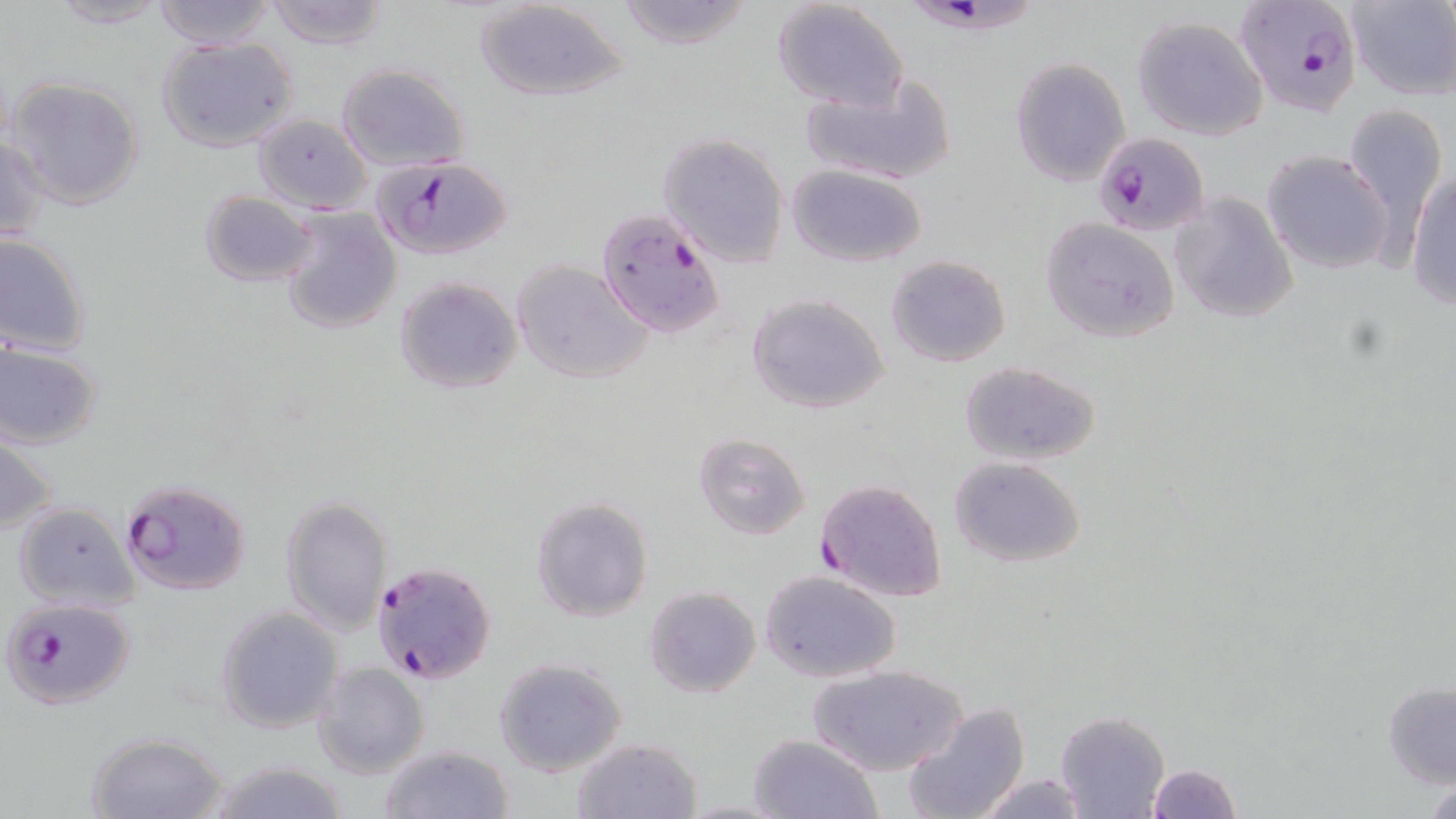
slide-level diagnosis = Plasmodium falciparum
modality = light microscopy
stain = May-Grünwald-Giemsa
magnification = 1000x
Plasmodium falciparum-infected red blood cell locations = approximate bounding boxes as named x1/y1/x2/y2 corners in pixels: (x1=910, y1=0, x2=1036, y2=40), (x1=1238, y1=0, x2=1364, y2=115), (x1=1098, y1=126, x2=1212, y2=239), (x1=373, y1=154, x2=516, y2=260), (x1=596, y1=207, x2=725, y2=338), (x1=814, y1=477, x2=948, y2=603), (x1=119, y1=479, x2=251, y2=597), (x1=369, y1=557, x2=496, y2=685), (x1=2, y1=597, x2=134, y2=710)
preparation = thin blood smear
image size = 1456×819 pixels
field of view = single
uninfected red blood cell locations = approximate bounding boxes as named x1/y1/x2/y2 corners in pixels: (x1=45, y1=0, x2=171, y2=28), (x1=151, y1=0, x2=277, y2=49), (x1=264, y1=0, x2=387, y2=49), (x1=472, y1=0, x2=631, y2=105), (x1=614, y1=0, x2=756, y2=50), (x1=1344, y1=1, x2=1456, y2=100), (x1=771, y1=2, x2=908, y2=111), (x1=1131, y1=14, x2=1269, y2=142), (x1=154, y1=36, x2=298, y2=152), (x1=1010, y1=57, x2=1130, y2=186), (x1=335, y1=63, x2=471, y2=172), (x1=800, y1=76, x2=957, y2=186), (x1=6, y1=77, x2=145, y2=212), (x1=1340, y1=101, x2=1445, y2=249), (x1=252, y1=114, x2=372, y2=212), (x1=657, y1=132, x2=791, y2=267), (x1=1, y1=134, x2=49, y2=243), (x1=1263, y1=150, x2=1393, y2=274), (x1=786, y1=164, x2=927, y2=267), (x1=1407, y1=165, x2=1456, y2=310), (x1=198, y1=189, x2=319, y2=287), (x1=1170, y1=192, x2=1299, y2=324), (x1=279, y1=207, x2=402, y2=335), (x1=1041, y1=220, x2=1180, y2=344), (x1=0, y1=232, x2=94, y2=358), (x1=886, y1=254, x2=1011, y2=368), (x1=512, y1=260, x2=654, y2=385), (x1=394, y1=277, x2=523, y2=394), (x1=747, y1=294, x2=889, y2=415), (x1=1, y1=340, x2=103, y2=450), (x1=957, y1=360, x2=1102, y2=466), (x1=693, y1=432, x2=811, y2=540), (x1=0, y1=435, x2=57, y2=536), (x1=947, y1=456, x2=1088, y2=568), (x1=280, y1=495, x2=392, y2=634), (x1=530, y1=495, x2=653, y2=623), (x1=13, y1=502, x2=136, y2=609), (x1=757, y1=569, x2=902, y2=683), (x1=643, y1=583, x2=761, y2=698), (x1=216, y1=607, x2=344, y2=735), (x1=494, y1=658, x2=627, y2=776), (x1=312, y1=663, x2=429, y2=780), (x1=809, y1=664, x2=968, y2=776), (x1=1382, y1=681, x2=1456, y2=790), (x1=901, y1=701, x2=1029, y2=819), (x1=1054, y1=711, x2=1171, y2=819), (x1=84, y1=730, x2=229, y2=819), (x1=746, y1=734, x2=883, y2=819), (x1=571, y1=737, x2=702, y2=818), (x1=379, y1=744, x2=515, y2=819), (x1=195, y1=760, x2=352, y2=819), (x1=1146, y1=763, x2=1241, y2=819), (x1=967, y1=772, x2=1095, y2=818), (x1=1422, y1=776, x2=1455, y2=818)